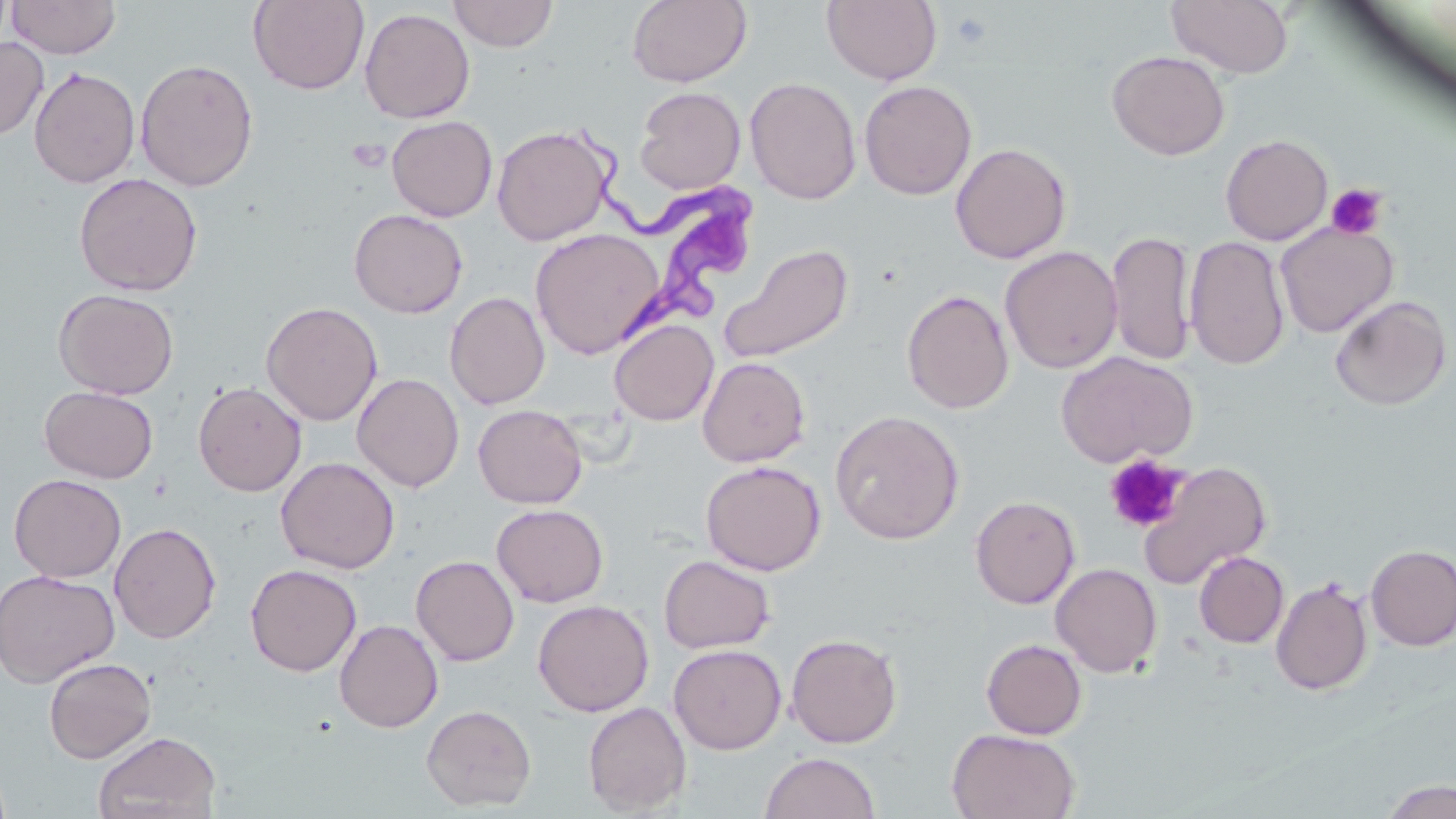
Summary:
  - Coordinate format: approximate bounding boxes as [x1, y1, x2, y2] in pixels
  - Trypanosoma brucei locations: [583, 127, 764, 344]
  - Uninfected red blood cell locations: [7, 0, 121, 60], [447, 0, 559, 51], [627, 0, 751, 87], [1166, 0, 1294, 79], [248, 1, 369, 94], [821, 1, 942, 85], [359, 8, 475, 123], [0, 36, 49, 140], [1107, 50, 1230, 160], [135, 58, 259, 191], [29, 67, 140, 188], [744, 77, 862, 205], [859, 79, 977, 200], [634, 87, 746, 194], [387, 115, 498, 222], [491, 124, 616, 246], [1221, 134, 1333, 245], [950, 142, 1071, 265], [74, 172, 203, 296], [349, 208, 468, 318], [1275, 221, 1398, 338], [530, 228, 666, 360], [1107, 229, 1196, 366], [1185, 235, 1290, 371], [720, 243, 854, 363], [1000, 245, 1123, 374], [53, 288, 179, 400], [901, 289, 1014, 414], [444, 291, 550, 410], [1329, 295, 1452, 411], [261, 301, 383, 426], [609, 319, 719, 426], [1056, 352, 1198, 468], [697, 356, 810, 467], [351, 373, 464, 492], [194, 381, 307, 496], [39, 385, 158, 483], [473, 404, 587, 508], [829, 409, 965, 545], [275, 456, 400, 574], [1138, 460, 1272, 590], [701, 461, 826, 575], [9, 474, 126, 583], [970, 495, 1080, 609], [491, 503, 609, 607], [109, 522, 221, 644], [1365, 544, 1456, 651], [1194, 551, 1289, 648], [659, 554, 776, 653], [411, 555, 519, 666], [1050, 562, 1162, 678], [245, 564, 362, 676], [0, 569, 119, 688], [1271, 578, 1372, 696], [532, 599, 654, 717], [334, 619, 443, 733], [786, 633, 902, 747], [981, 638, 1087, 740], [668, 643, 787, 754], [43, 657, 157, 764], [583, 701, 692, 816], [421, 704, 537, 811], [947, 728, 1081, 819], [93, 730, 221, 819], [759, 751, 881, 818], [1381, 780, 1456, 819]
  - Platelet locations: [346, 138, 390, 174], [1325, 183, 1388, 240], [1104, 453, 1189, 534]
  - Slide-level diagnosis: Trypanosoma brucei
  - Stain: May-Grünwald-Giemsa
  - Image size: 1456×819 pixels
  - Modality: optical microscopy
  - Field of view: one of a larger specimen
  - Preparation: thin blood smear
  - Magnification: 1000x